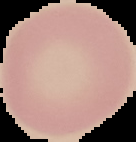

{
  "image_type": "cell region segmented out of the field of view; surrounding area masked to black",
  "malaria_status": "uninfected",
  "preparation": "thin blood film",
  "image_size": "136×142 pixels"
}